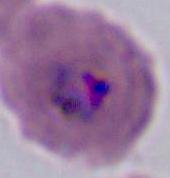

Summary:
  - Magnification: 400x or 1000x
  - Identification: Plasmodium
  - Modality: photomicrograph